Identify the parasite.
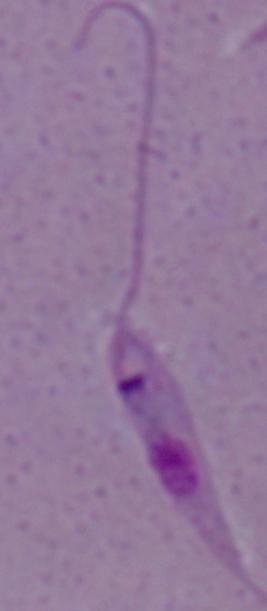
This is Leishmania.

Photomicrograph. 1000x magnification.